Name the blood parasite species.
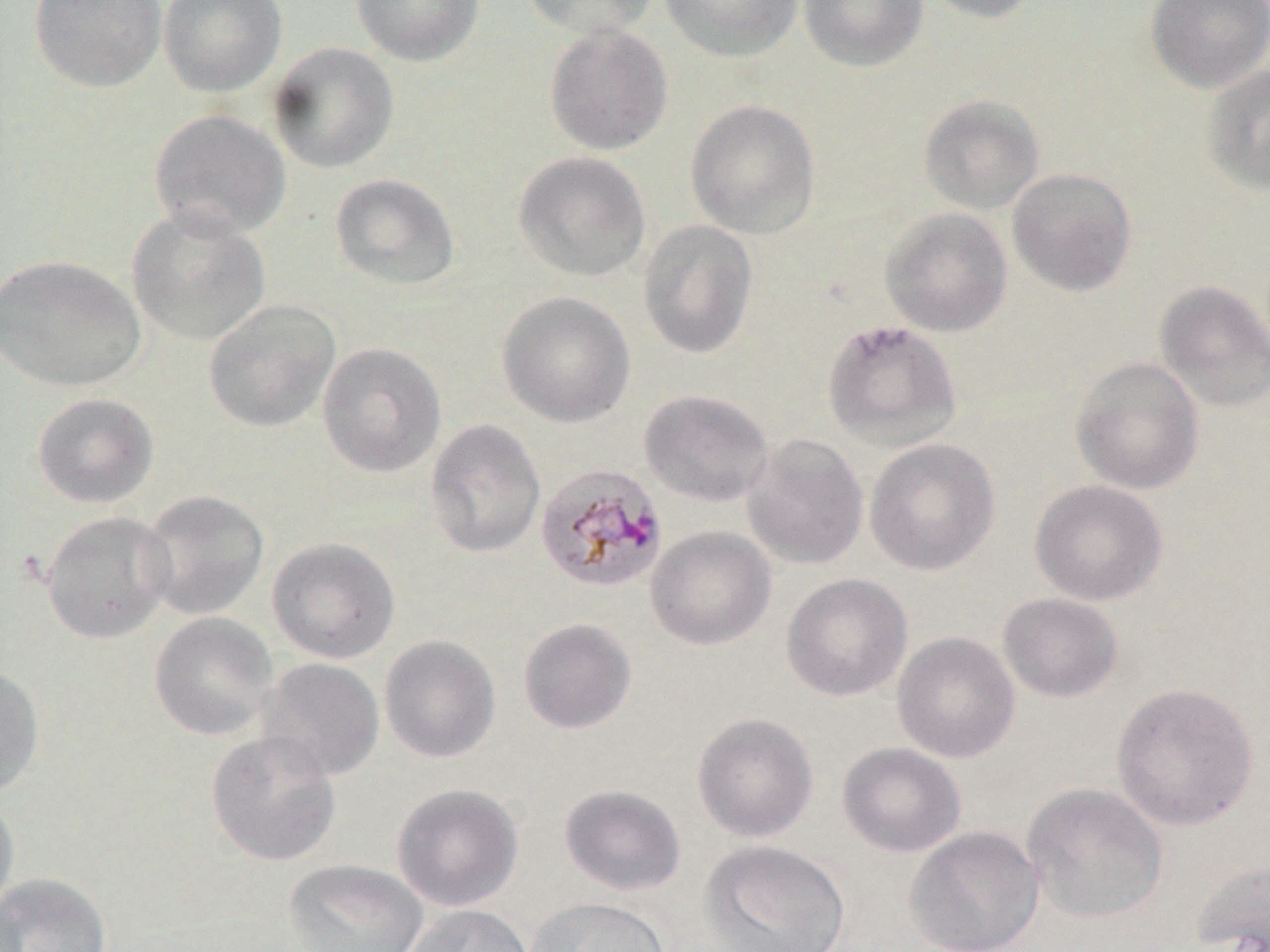
Plasmodium malariae.

Approximate bounding boxes as (x1, y1, x2, y2) in pixels. Uninfected red blood cell locations: (29, 0, 165, 92), (158, 0, 287, 97), (351, 0, 485, 66), (520, 0, 659, 40), (660, 0, 802, 62), (798, 0, 928, 71), (918, 0, 1044, 23), (1145, 0, 1270, 93), (543, 24, 673, 156), (267, 41, 399, 174), (1201, 63, 1270, 196), (918, 94, 1045, 215), (684, 99, 822, 239), (149, 109, 291, 240), (513, 151, 652, 282), (1006, 168, 1137, 297), (329, 173, 461, 291), (126, 207, 271, 346), (879, 207, 1013, 337), (637, 219, 759, 360), (1, 254, 146, 392), (1154, 280, 1270, 413), (497, 291, 636, 428), (203, 299, 341, 432), (822, 320, 962, 452), (317, 342, 447, 478), (1070, 356, 1205, 495), (638, 390, 775, 507), (32, 392, 159, 509), (425, 418, 546, 558), (742, 433, 869, 570), (864, 437, 1000, 577), (1029, 478, 1168, 606), (137, 489, 270, 620), (39, 511, 176, 644), (645, 525, 777, 651), (266, 537, 401, 664), (781, 573, 913, 702), (997, 593, 1124, 703), (148, 612, 278, 741), (518, 618, 637, 734), (892, 630, 1020, 763), (378, 635, 501, 763), (257, 657, 385, 782), (0, 661, 45, 797), (1111, 682, 1259, 831), (692, 713, 819, 842), (206, 729, 342, 866), (837, 742, 966, 857), (1021, 782, 1168, 923), (391, 783, 524, 912), (558, 784, 687, 896), (0, 792, 20, 918), (905, 826, 1045, 952), (700, 840, 852, 952), (284, 859, 428, 952), (1191, 859, 1270, 951), (0, 872, 112, 952), (525, 895, 672, 952), (403, 904, 534, 952). Plasmodium malariae-infected red blood cell locations: (535, 463, 668, 593). Single field of view. May-Grünwald-Giemsa stain. Thin blood film. Captured at 1000x magnification. Light microscopy. Image is 1270×952 pixels.